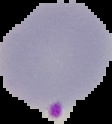

The area outside the segmented cell region is set to black. From a thin blood film. Result: malaria parasites detected. Image is 112×124 pixels.